Point out each malaria parasite.
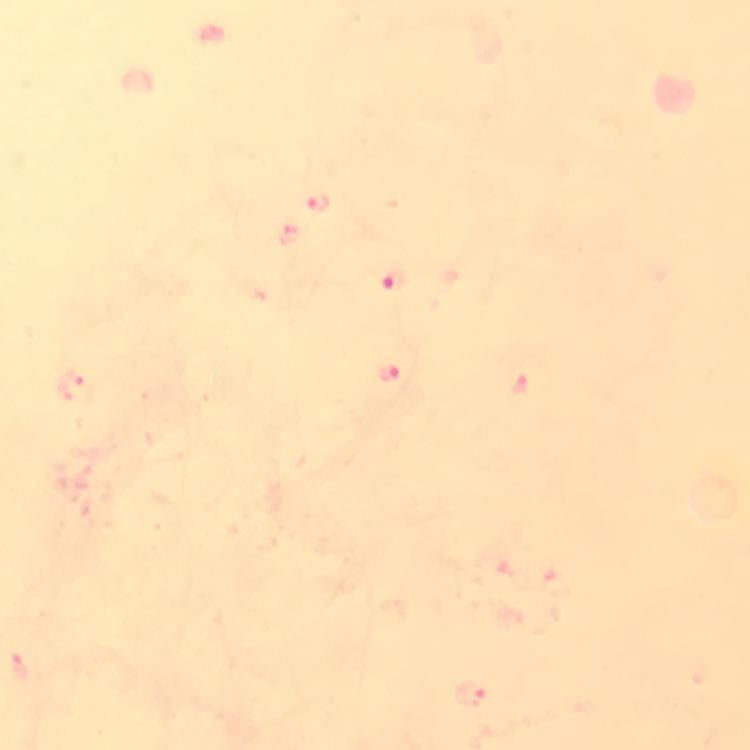

Approximate object centers, in pixels from the top-left corner.
Malaria parasites: (x=318, y=203), (x=293, y=236), (x=396, y=280), (x=393, y=370), (x=76, y=384), (x=471, y=696).

magnification: 100x
immersion_oil: used
cropped_from: one field of view
preparation: thick blood film
capture: smartphone camera through the microscope
image_size: 750×750 pixels
context: from a malaria diagnostic workup
stain: Giemsa